Identify the preparation type.
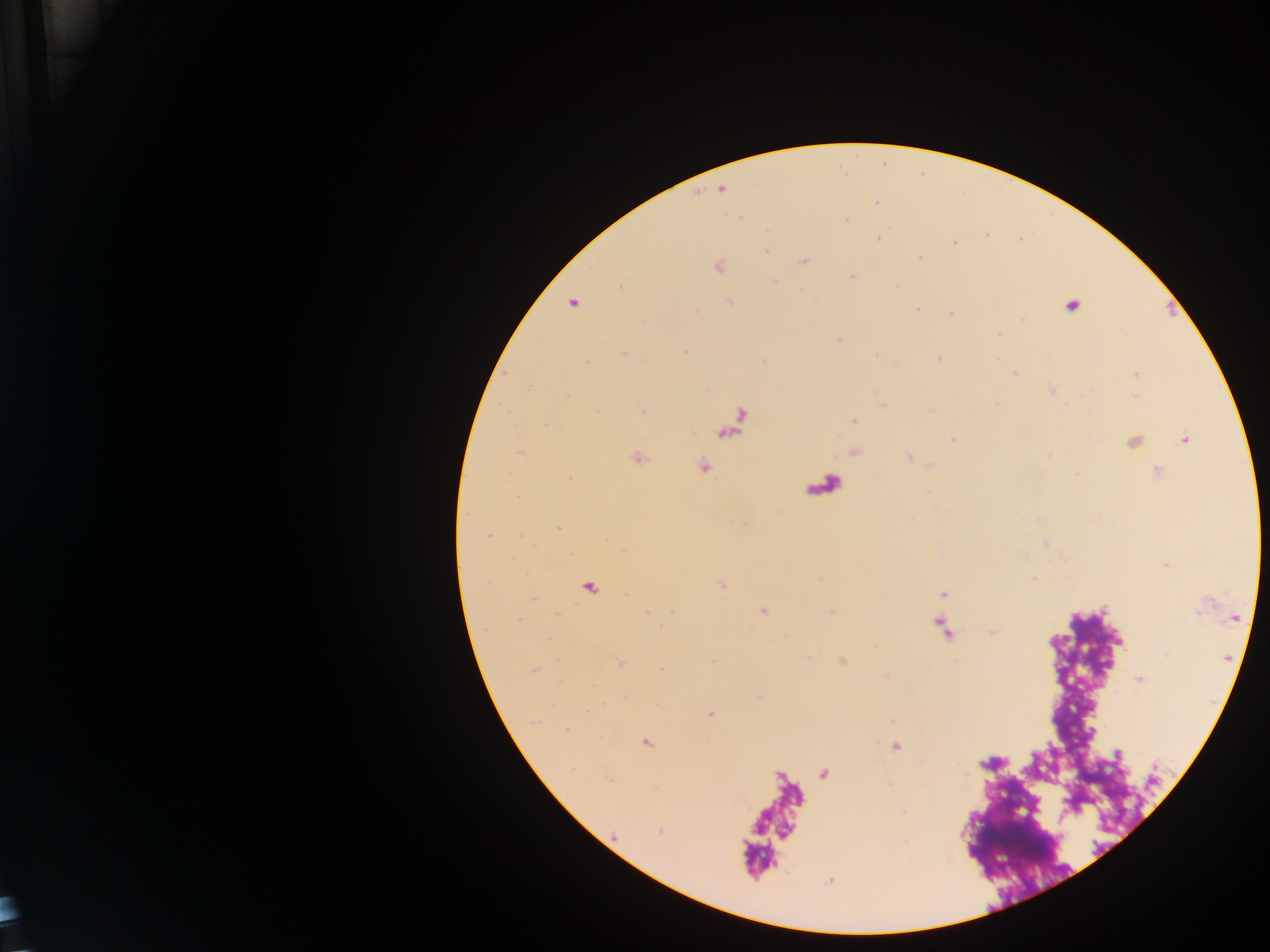

Thick blood film.

malaria parasite locations = approximate centers as x y in pixels: 720 189; 876 204; 847 221; 879 238; 954 243; 766 252; 921 258; 805 261; 719 266; 852 277; 774 282; 620 286; 730 302; 572 303; 1072 306; 918 309; 951 314; 1023 321; 998 334; 840 339; 685 351; 624 354; 938 358; 586 363; 1015 373; 1137 373; 528 388; 568 396; 883 406; 643 412; 853 420; 546 425; 953 438; 1185 440; 519 452; 637 458; 703 466; 1156 471; 1077 474; 571 479; 558 528; 489 537; 1034 578; 943 593; 673 612; 763 612; 646 613; 518 620; 621 662; 661 669; 535 670; 1140 679; 710 714; 567 730; 647 742; 895 746; 1118 754; 610 779; 904 812; 660 831
country = Ghana
image size = 1270×952 pixels
field of view = single
capture = mobile-phone photograph through a microscope